Locate every Plasmodium malariae-infected red blood cell.
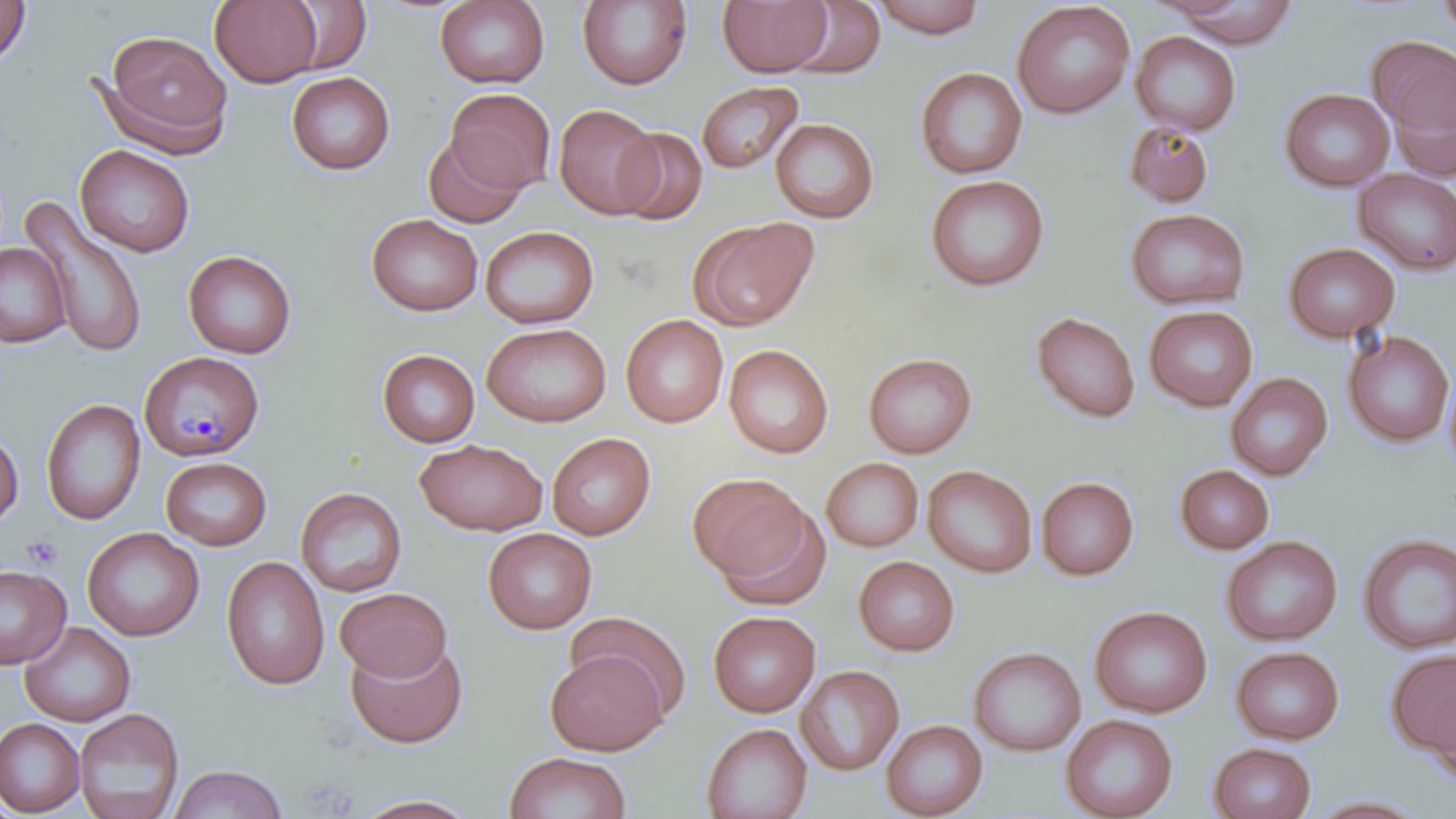

Approximate bounding boxes as [x1, y1, x2, y2] in pixels.
Plasmodium malariae-infected red blood cells: [139, 351, 264, 460].

slide_level_diagnosis: Plasmodium malariae
modality: light microscopy
platelet_locations: 'approximate bounding boxes as [x1, y1, x2, y2] in pixels: [23, 535, 63, 570], [299, 776, 358, 816]'
stain: May-Grünwald-Giemsa
uninfected_red_blood_cell_locations: 'approximate bounding boxes as [x1, y1, x2, y2] in pixels: [0, 0, 32, 67], [209, 0, 323, 87], [280, 0, 373, 75], [434, 0, 550, 90], [716, 0, 833, 77], [870, 0, 988, 39], [1435, 0, 1456, 39], [576, 1, 693, 91], [786, 1, 887, 80], [1012, 1, 1135, 119], [1161, 1, 1302, 47], [100, 29, 233, 155], [1130, 31, 1242, 137], [1368, 35, 1456, 138], [914, 67, 1028, 179], [286, 71, 395, 175], [1386, 75, 1456, 183], [696, 81, 804, 174], [1279, 87, 1394, 192], [446, 88, 556, 193], [553, 103, 663, 219], [770, 117, 880, 223], [1123, 119, 1215, 208], [612, 126, 708, 225], [423, 132, 528, 228], [74, 144, 195, 257], [1353, 168, 1456, 276], [925, 174, 1050, 292], [20, 199, 150, 360], [1124, 207, 1250, 311], [366, 214, 482, 316], [689, 217, 819, 332], [480, 225, 599, 329], [0, 242, 71, 349], [1282, 242, 1400, 344], [182, 249, 297, 359], [1144, 305, 1258, 412], [1030, 311, 1141, 423], [621, 314, 728, 428], [481, 323, 612, 427], [1342, 330, 1454, 447], [723, 344, 834, 459], [377, 349, 480, 447], [863, 352, 977, 458], [1443, 365, 1456, 482], [1225, 372, 1333, 481], [40, 398, 146, 526], [0, 427, 23, 529], [547, 432, 655, 540], [415, 438, 548, 536], [161, 456, 272, 550], [821, 457, 923, 552], [922, 464, 1037, 578], [1174, 465, 1274, 554], [687, 472, 813, 586], [1036, 476, 1139, 581], [295, 487, 408, 597], [715, 506, 834, 612], [82, 526, 204, 642], [483, 528, 597, 634], [1358, 534, 1456, 655], [1221, 536, 1343, 646], [221, 556, 330, 691], [853, 556, 959, 656], [0, 564, 71, 670], [334, 587, 453, 682], [1089, 605, 1212, 718], [707, 610, 821, 718], [565, 611, 692, 721], [19, 622, 136, 727], [345, 640, 468, 749], [968, 646, 1086, 756], [1231, 646, 1344, 745], [1386, 648, 1456, 758], [545, 650, 669, 756], [796, 665, 904, 776], [1428, 687, 1456, 787], [73, 708, 185, 819], [1061, 714, 1178, 819], [0, 717, 85, 817], [880, 719, 988, 819], [701, 722, 812, 819], [1207, 742, 1316, 819], [503, 751, 632, 819], [169, 764, 288, 819], [349, 794, 481, 818], [1303, 794, 1433, 818]'
preparation: thin blood smear
image_size: 1456×819 pixels
field_of_view: single
magnification: 1000x